Report the malaria status of this cell.
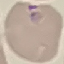
Parasitized.

image type = cell patch, automatically extracted from a larger field of view and resized to 64 × 64 pixels
capture = smartphone camera at the microscope eyepiece
stain = Giemsa
preparation = thin blood smear